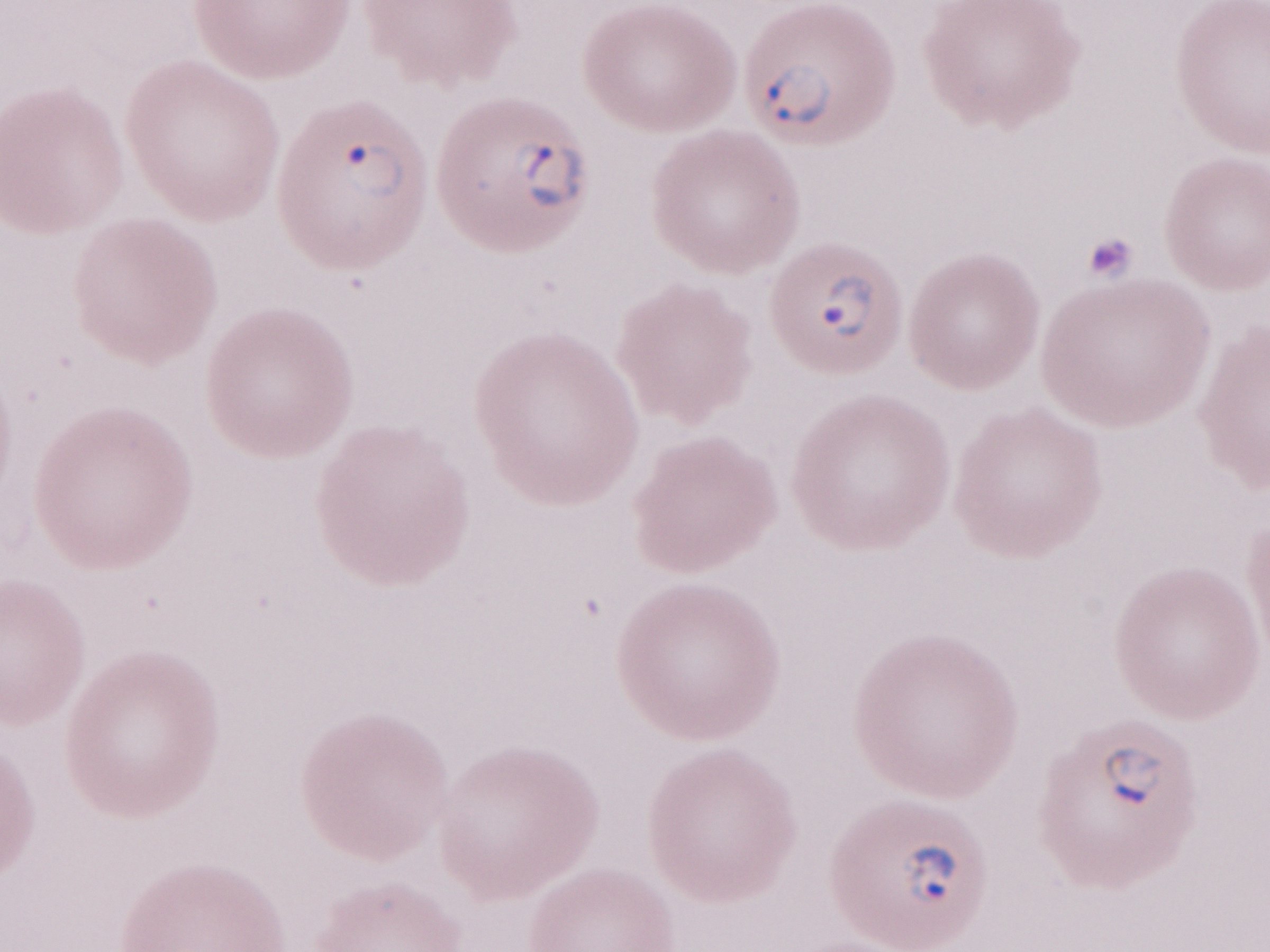

Olympus BX43 microscope, Olympus DP73 camera. 1,000x magnification. May-Grünwald-Giemsa-stained preparation. One field of this slide. Thin blood smear. Image is 1270×952 pixels. Malaria diagnosis (patient-level): positive.